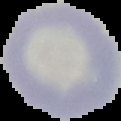
Image is 121×121 pixels. Cell region segmented out of the field of view; the surrounding area is masked to black. From a thin blood smear. Result: no malaria parasites detected.